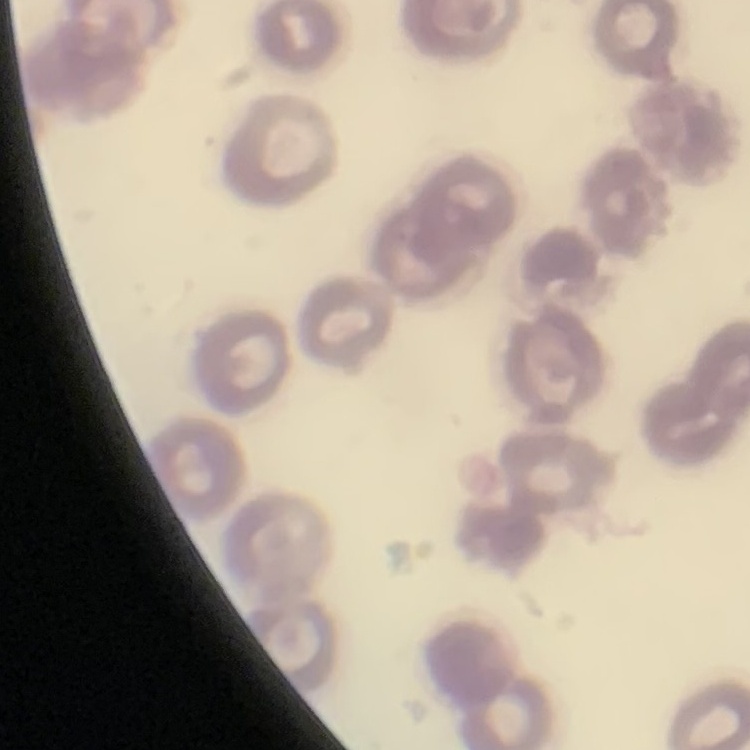
erythrocyte morphology = no rouleaux formation
preparation = thin blood film
image type = square crop of a larger photomicrograph
stain = Field's or Giemsa